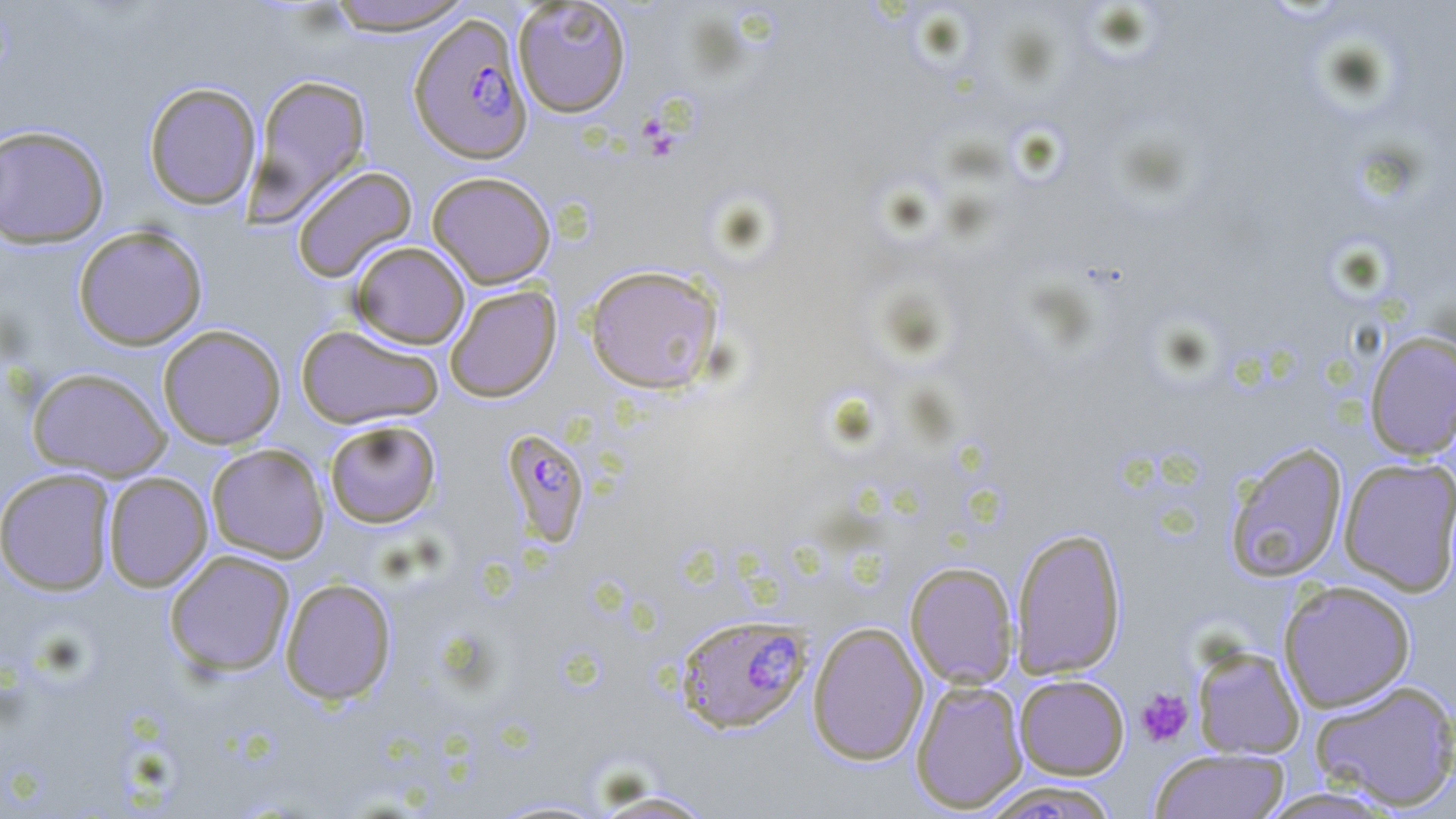
slide_level_diagnosis: Plasmodium falciparum
magnification: 1000x
modality: light microscopy
image_size: 1456×819 pixels
platelet_locations: 'approximate bounding boxes as [x1, y1, x2, y2] in pixels: [639, 117, 665, 140], [649, 143, 676, 163], [1136, 688, 1194, 747]'
field_of_view: single
plasmodium_falciparum_infected_red_blood_cell_locations: 'approximate bounding boxes as [x1, y1, x2, y2] in pixels: [408, 13, 534, 164], [499, 428, 591, 548], [674, 614, 811, 734], [976, 780, 1124, 818]'
uninfected_red_blood_cell_locations: 'approximate bounding boxes as [x1, y1, x2, y2] in pixels: [321, 0, 477, 36], [512, 0, 632, 117], [246, 73, 372, 222], [143, 82, 261, 210], [0, 124, 110, 248], [291, 165, 418, 283], [426, 171, 556, 289], [73, 225, 208, 350], [350, 241, 470, 349], [583, 264, 724, 395], [444, 284, 561, 403], [158, 324, 287, 450], [296, 324, 444, 430], [1364, 330, 1456, 461], [27, 367, 172, 482], [324, 419, 442, 528], [1224, 442, 1348, 583], [206, 444, 329, 563], [1338, 457, 1456, 596], [0, 468, 117, 595], [102, 472, 213, 591], [1010, 526, 1127, 680], [164, 549, 296, 677], [905, 561, 1019, 689], [280, 578, 397, 705], [1278, 580, 1416, 712], [807, 621, 929, 765], [1191, 645, 1306, 760], [1014, 674, 1129, 779], [1309, 678, 1456, 812], [910, 679, 1028, 814], [1150, 747, 1289, 819], [587, 789, 721, 818], [487, 797, 615, 818]'
preparation: thin blood smear
stain: May-Grünwald-Giemsa